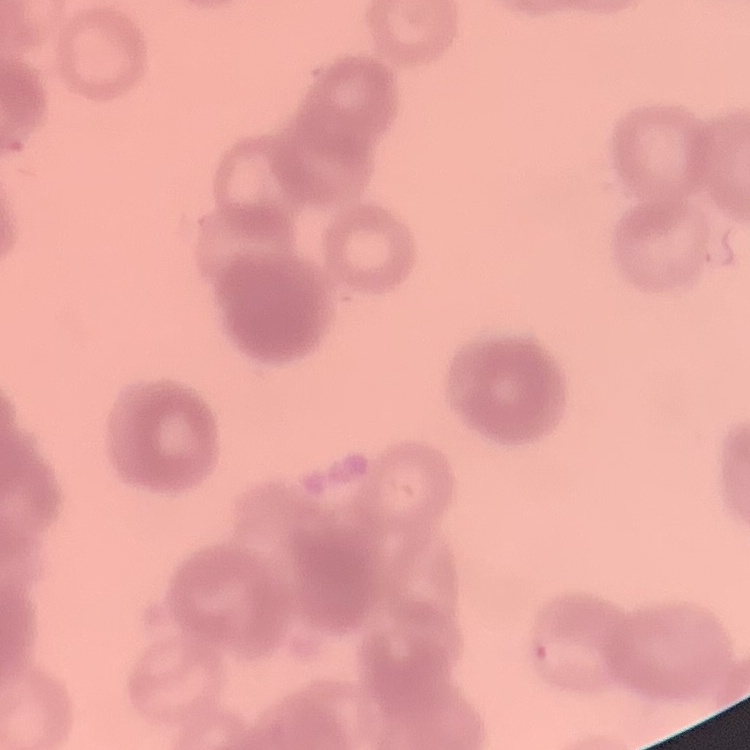

{
  "erythrocyte_morphology": "rouleaux formation",
  "preparation": "thin blood smear",
  "stain": "Field's or Giemsa",
  "image_type": "square crop of a larger photomicrograph"
}